Identify the parasite.
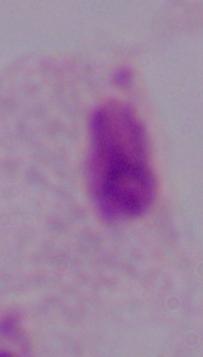
This is a trichomonad.

1000x magnification. Micrograph.